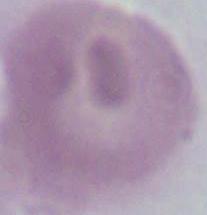

Summary:
  - Magnification: 1000x
  - Identification: red blood cell
  - Modality: micrograph